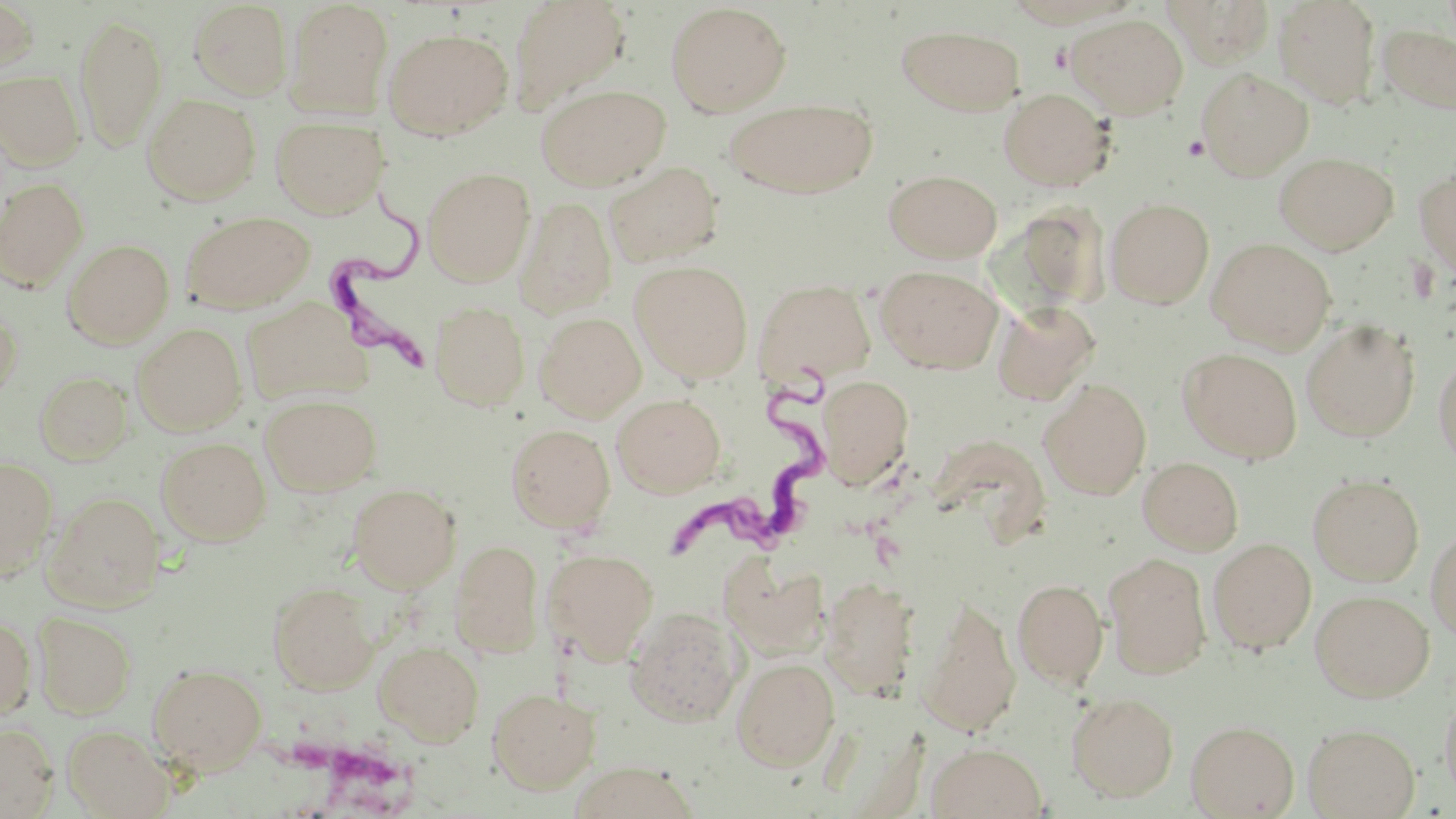
Summary:
  - Coordinate format: approximate bounding boxes as [x1, y1, x2, y2] in pixels
  - Uninfected red blood cell locations: [506, 0, 632, 115], [1163, 0, 1276, 66], [1272, 0, 1382, 108], [188, 1, 292, 100], [284, 1, 393, 118], [0, 2, 40, 78], [665, 2, 791, 117], [73, 13, 168, 150], [1067, 14, 1189, 119], [897, 25, 1025, 115], [1379, 25, 1456, 114], [383, 27, 513, 140], [1196, 68, 1313, 180], [0, 69, 85, 171], [537, 83, 669, 191], [998, 88, 1114, 191], [142, 93, 260, 205], [725, 97, 877, 199], [271, 116, 387, 218], [1274, 152, 1399, 254], [605, 161, 723, 267], [1414, 164, 1456, 276], [422, 167, 535, 286], [883, 168, 1002, 262], [0, 178, 88, 290], [514, 197, 617, 320], [1106, 198, 1214, 308], [180, 210, 316, 313], [1208, 237, 1336, 354], [62, 238, 174, 348], [630, 260, 754, 383], [875, 265, 1002, 373], [753, 279, 876, 386], [242, 300, 367, 405], [992, 300, 1100, 406], [429, 301, 530, 411], [0, 309, 22, 408], [535, 312, 646, 421], [1301, 318, 1421, 443], [132, 323, 246, 435], [1178, 347, 1303, 463], [1433, 350, 1456, 473], [35, 371, 133, 465], [815, 374, 914, 487], [1039, 378, 1152, 499], [612, 393, 726, 497], [260, 394, 381, 496], [506, 424, 615, 532], [157, 437, 271, 544], [0, 456, 59, 578], [1137, 456, 1244, 556], [1308, 473, 1425, 586], [348, 483, 461, 593], [44, 491, 165, 613], [1425, 524, 1456, 642], [1207, 537, 1317, 654], [450, 540, 543, 657], [544, 548, 659, 662], [1103, 552, 1212, 678], [721, 556, 829, 659], [821, 576, 921, 699], [1012, 578, 1108, 690], [268, 582, 379, 694], [1310, 589, 1434, 701], [918, 594, 1021, 737], [624, 606, 745, 726], [32, 612, 136, 720], [0, 617, 36, 719], [374, 641, 484, 746], [731, 657, 840, 771], [148, 664, 267, 774], [487, 688, 601, 793], [1439, 688, 1456, 803], [1067, 692, 1179, 802], [1186, 720, 1299, 817], [0, 722, 59, 817], [1302, 723, 1419, 818], [63, 725, 174, 819], [926, 742, 1048, 818], [566, 762, 700, 819]
  - Trypanosoma brucei locations: [326, 187, 456, 372], [666, 348, 835, 570]
  - Platelet locations: [1182, 136, 1210, 160]
  - Slide-level diagnosis: Trypanosoma brucei
  - Magnification: 1000x
  - Preparation: thin blood smear
  - Image size: 1456×819 pixels
  - Modality: light microscopy
  - Stain: May-Grünwald-Giemsa
  - Field of view: single